Assess this cell for malaria.
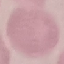

It is uninfected.

Summary:
  - Stain: Giemsa
  - Capture: smartphone camera at the microscope eyepiece
  - Image type: automatically extracted cell patch, resized to 64 × 64 pixels
  - Preparation: thin blood smear